Comment on the morphology of the red blood cells.
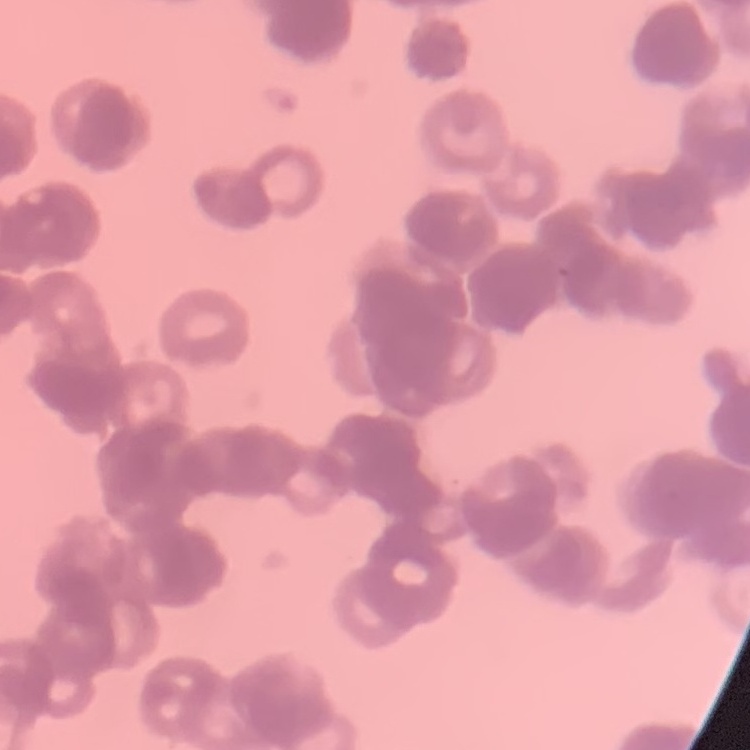
They show rouleaux formation.

Summary:
  - Image type: one tile cut from a larger photomicrograph
  - Stain: Field's or Giemsa
  - Preparation: thin blood smear